Locate every blood parasite and identify its species.
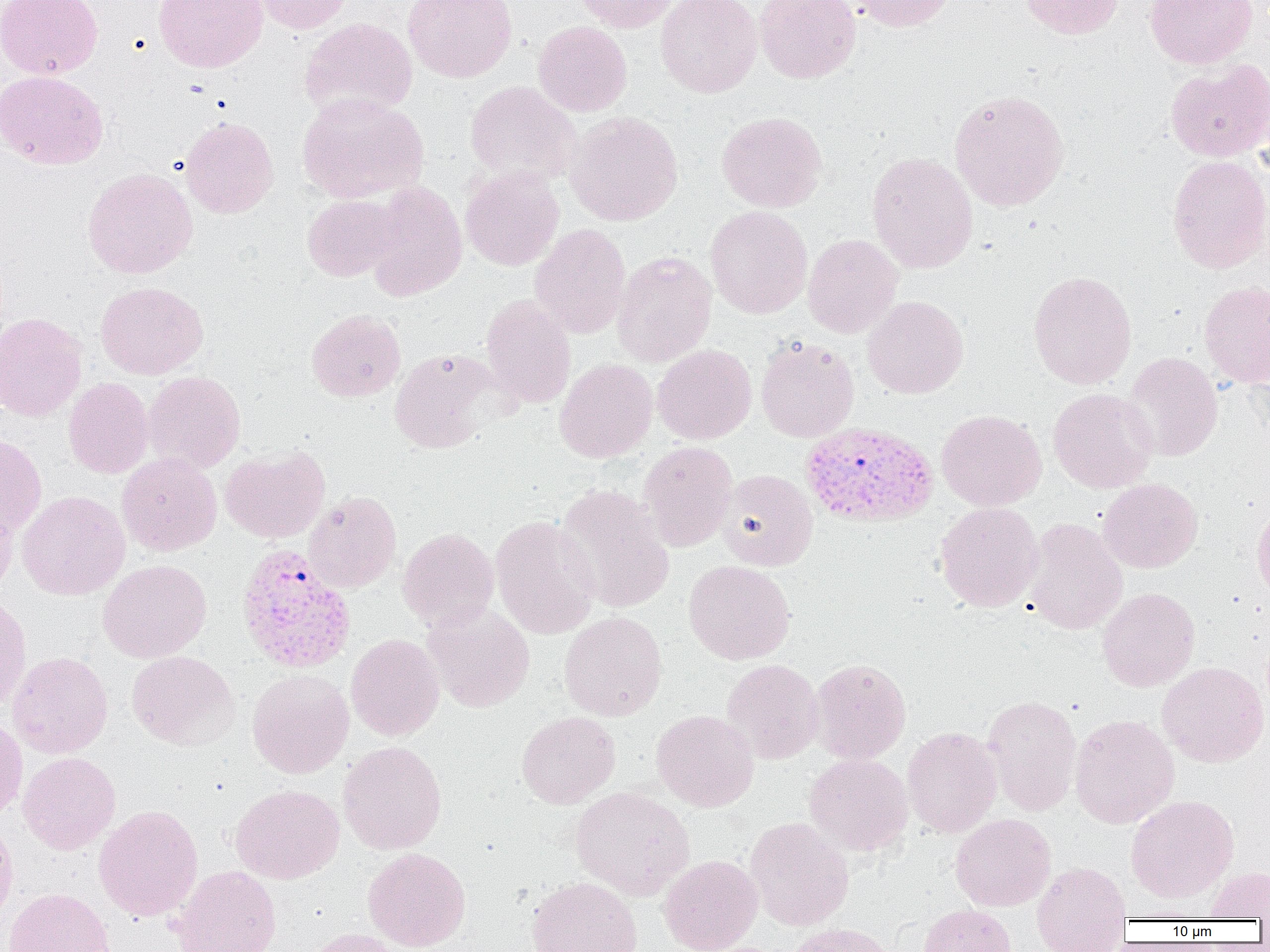

Approximate bounding boxes as (x1, y1, x2, y2) in pixels.
Plasmodium vivax-infected red blood cells: (799, 421, 939, 528), (237, 542, 357, 673).
No Plasmodium falciparum, Plasmodium ovale, Plasmodium malariae, Babesia divergens, or Trypanosoma brucei observed.

Uninfected red blood cell locations: (0, 0, 102, 79), (153, 0, 267, 72), (250, 0, 356, 34), (403, 0, 517, 83), (573, 0, 680, 32), (655, 0, 763, 97), (755, 0, 861, 83), (849, 0, 954, 32), (1019, 0, 1124, 39), (1145, 0, 1258, 69), (299, 17, 418, 120), (533, 21, 632, 116), (1165, 60, 1270, 162), (0, 70, 109, 169), (464, 81, 582, 187), (949, 89, 1070, 212), (297, 92, 429, 203), (717, 110, 828, 213), (565, 111, 683, 226), (180, 116, 279, 218), (867, 151, 978, 273), (1167, 155, 1270, 274), (460, 166, 564, 271), (83, 167, 198, 278), (362, 181, 468, 301), (303, 194, 402, 281), (705, 206, 813, 319), (529, 224, 631, 339), (802, 234, 903, 338), (611, 251, 717, 367), (1028, 270, 1137, 389), (96, 281, 208, 379), (1199, 281, 1270, 388), (480, 294, 576, 408), (863, 296, 969, 398), (306, 309, 406, 402), (0, 312, 87, 422), (755, 337, 859, 442), (652, 345, 757, 445), (389, 348, 501, 454), (1122, 352, 1222, 461), (554, 358, 658, 463), (143, 371, 246, 473), (64, 378, 154, 478), (1047, 387, 1158, 493), (936, 409, 1046, 511), (0, 434, 46, 537), (638, 441, 739, 552), (220, 445, 330, 543), (117, 452, 222, 556), (717, 469, 819, 571), (1098, 478, 1203, 573), (554, 484, 676, 613), (17, 490, 130, 600), (304, 491, 402, 593), (0, 496, 18, 600), (934, 502, 1044, 612), (1251, 502, 1270, 604), (490, 515, 600, 639), (1024, 518, 1127, 635), (398, 527, 499, 631), (98, 560, 212, 663), (684, 560, 795, 665), (1097, 587, 1200, 692), (0, 592, 31, 711), (422, 602, 535, 712), (559, 611, 667, 720), (345, 634, 444, 741), (127, 650, 240, 750), (8, 651, 112, 759), (808, 658, 912, 764), (722, 659, 823, 764), (1157, 661, 1269, 767), (247, 669, 354, 778), (982, 694, 1082, 816), (651, 710, 759, 811), (517, 711, 620, 808), (0, 714, 27, 819), (1070, 714, 1180, 829), (902, 726, 1002, 837), (338, 741, 447, 854), (18, 752, 120, 854), (804, 753, 913, 855), (230, 784, 344, 884), (570, 786, 695, 900), (1125, 795, 1239, 903), (94, 805, 203, 921), (950, 813, 1055, 911), (745, 816, 854, 931), (0, 817, 18, 929), (362, 847, 471, 951), (658, 854, 763, 952), (1032, 860, 1132, 949), (171, 865, 282, 952), (1203, 865, 1270, 920), (526, 876, 643, 952), (4, 888, 115, 952), (918, 904, 1016, 952), (785, 923, 895, 952), (304, 928, 409, 952). Slide-level diagnosis: Plasmodium vivax. Thin blood smear. One field of a larger specimen. 1000x magnification. Light microscopy. Image is 1270×952 pixels.